Name the parasite shown.
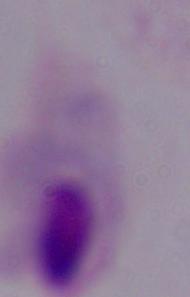
A trichomonad.

magnification = 1000x
modality = photomicrograph